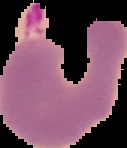

Result: Plasmodium parasites identified. The area outside the segmented cell region is set to black. From a thin blood smear. Image is 127×148 pixels.